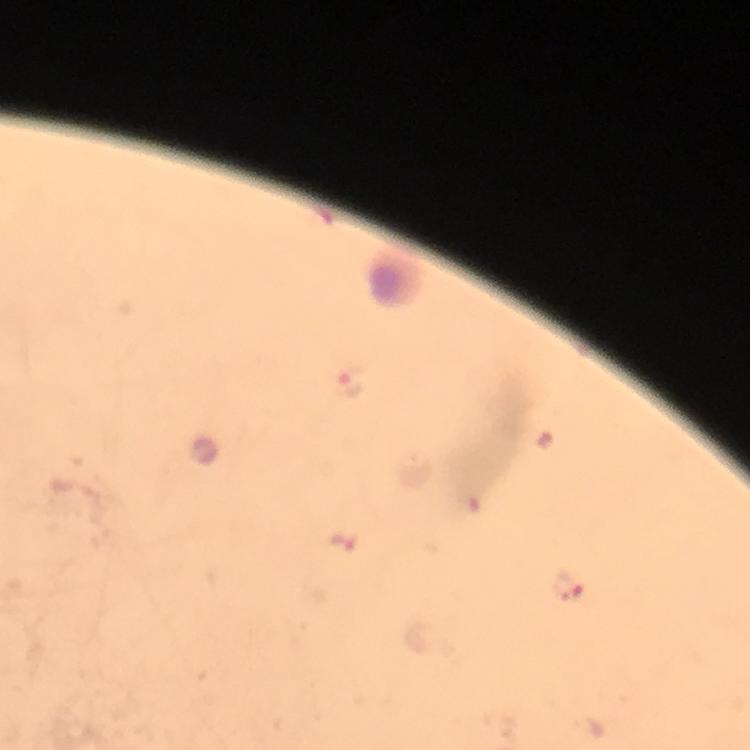

context = from a diagnostic examination for malaria
magnification = 100x
stain = Giemsa
malaria parasite locations = approximate object centers, in pixels from the top-left corner: (x=349, y=381), (x=345, y=544), (x=570, y=587)
image size = 750×750 pixels
capture = smartphone mounted on the microscope
preparation = thick smear
cropped from = one field of view
immersion oil = applied